Assess this cell for malaria.
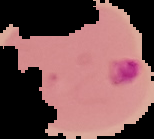
It is parasitized.

Summary:
  - Image type: segmented cell region on a black background
  - Image size: 154×139 pixels
  - Preparation: thin blood smear